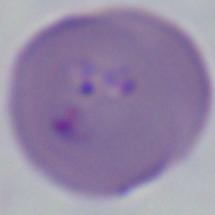

{
  "magnification": "1000x",
  "identification": "Babesia",
  "modality": "photomicrograph"
}